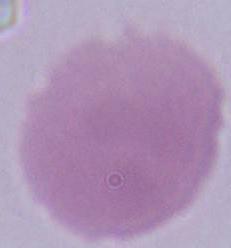

Summary:
  - Magnification: 1000x
  - Identification: erythrocyte
  - Modality: photomicrograph